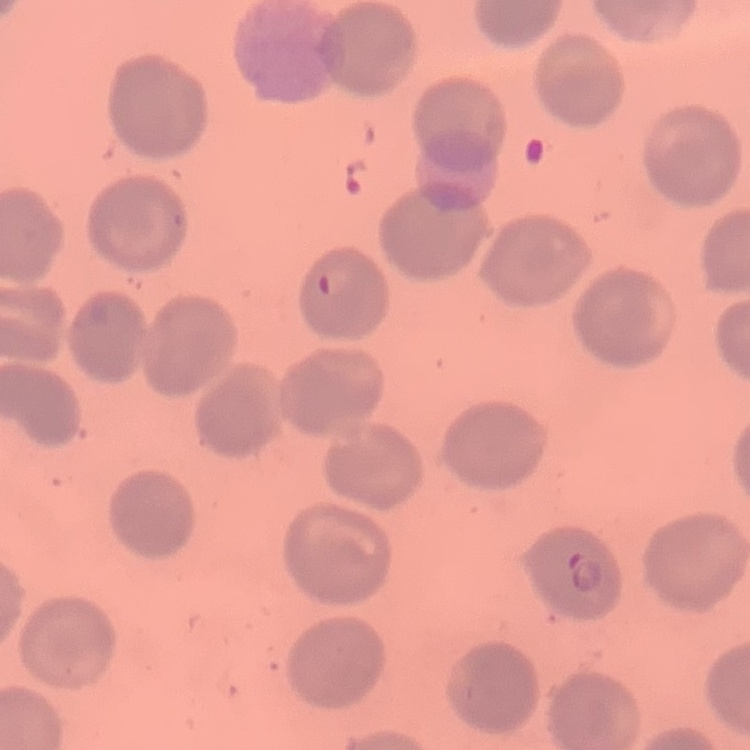

Summary:
  - Red blood cell morphology: no rouleaux formation
  - Image type: one tile cut from a larger photomicrograph
  - Preparation: thin peripheral smear
  - Stain: Field's or Giemsa